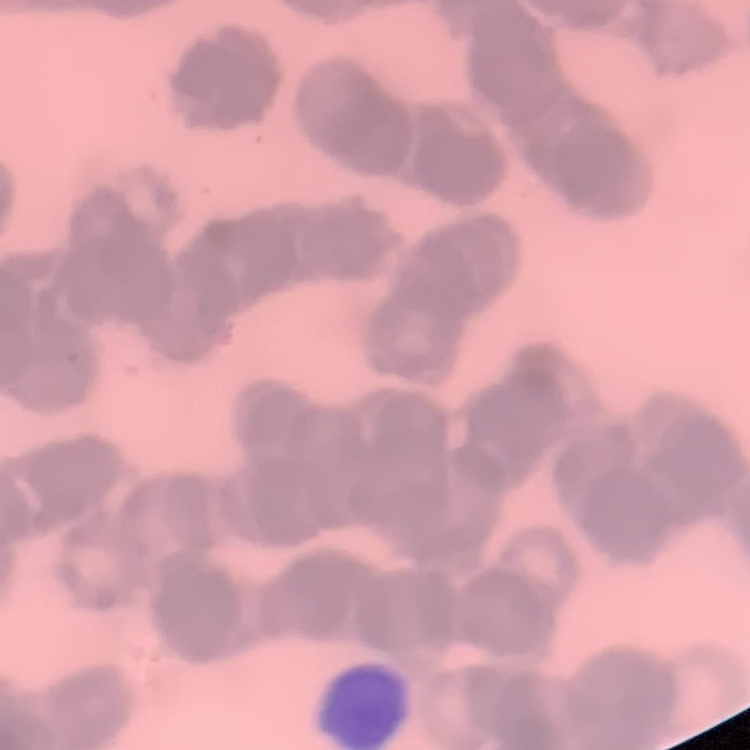
Summary:
  - Red blood cell morphology: rouleaux formation
  - Image type: square crop of a larger photomicrograph
  - Preparation: thin peripheral smear
  - Stain: Field's or Giemsa